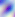 Photomicrograph. Captured at 400x magnification. Toxoplasma gondii is seen.